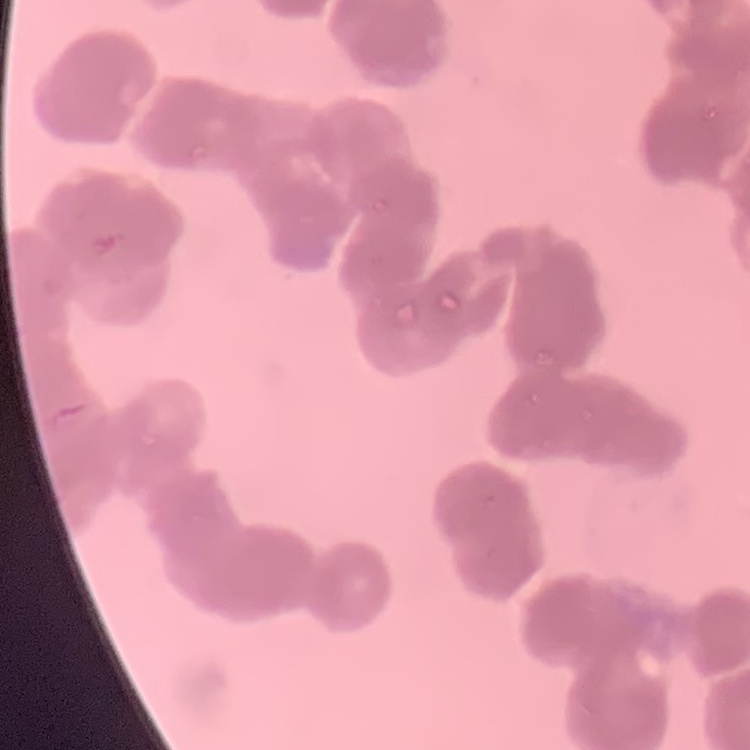

The erythrocytes exhibit rouleaux formation. Stained with either Field's or Giemsa. One tile cut from a larger photomicrograph. Thin blood smear.